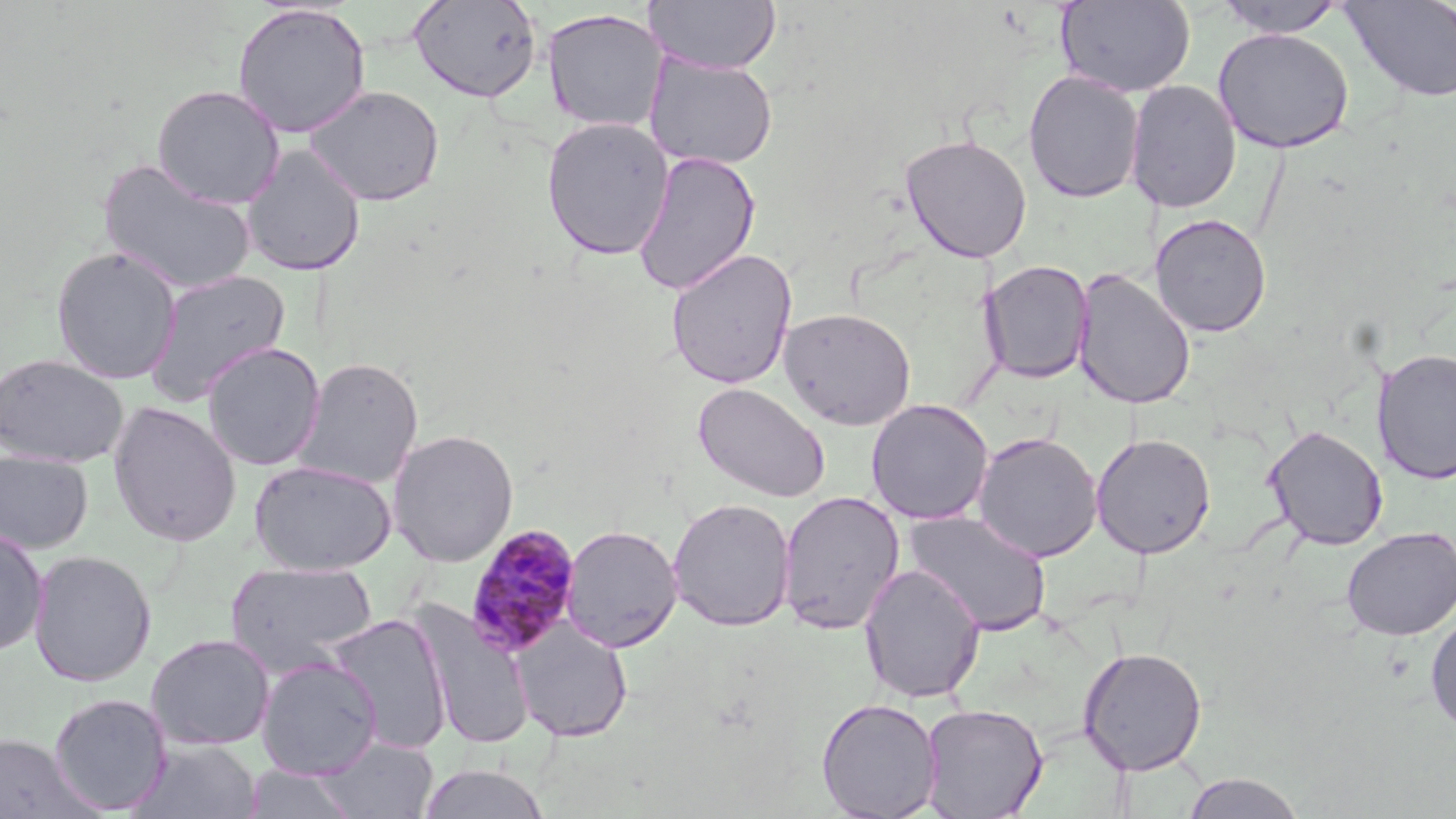

Approximate bounding boxes as (x1,y1)-(x2,y2) corner pairs in pixels. Plasmodium malariae-infected red blood cell locations: (464,525)-(582,658). Uninfected red blood cell locations: (644,0)-(781,74), (1056,0)-(1195,98), (1210,0)-(1350,38), (1339,0)-(1456,104), (407,1)-(543,103), (232,3)-(371,138), (542,8)-(669,134), (1213,27)-(1355,153), (644,53)-(778,171), (1023,69)-(1144,204), (1125,79)-(1242,213), (151,84)-(286,209), (304,85)-(445,207), (541,116)-(675,260), (899,133)-(1033,263), (241,146)-(366,277), (632,150)-(762,297), (98,159)-(256,295), (1150,213)-(1273,339), (50,246)-(182,384), (665,248)-(798,389), (978,260)-(1093,384), (142,268)-(292,408), (1071,268)-(1197,410), (778,307)-(916,430), (202,342)-(325,470), (1373,347)-(1456,484), (0,353)-(129,468), (293,357)-(424,489), (693,381)-(831,503), (865,399)-(994,525), (107,401)-(242,547), (1263,424)-(1388,551), (388,429)-(519,566), (972,432)-(1103,562), (1090,433)-(1216,559), (0,450)-(94,554), (249,459)-(396,576), (777,489)-(906,635), (667,497)-(796,631), (903,510)-(1052,636), (561,524)-(683,652), (0,525)-(49,657), (1341,526)-(1456,640), (28,549)-(157,687), (225,561)-(379,676), (859,562)-(986,703), (410,600)-(535,751), (1424,609)-(1456,735), (327,613)-(453,754), (512,618)-(633,743), (146,633)-(275,751), (1077,645)-(1207,775), (256,656)-(383,778), (48,693)-(172,815), (816,698)-(942,819), (919,702)-(1049,818), (0,734)-(96,819), (314,736)-(439,819), (129,738)-(263,819), (240,764)-(361,819), (417,764)-(551,819), (1181,771)-(1305,818). Slide-level diagnosis: Plasmodium malariae. May-Grünwald-Giemsa-stained preparation. Image is 1456×819 pixels. 1000x magnification. One field of a larger specimen. Light microscopy. Thin blood film.